Report the malaria status of this cell.
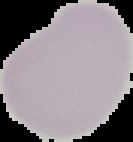
It is uninfected.

Cell region segmented out of the field of view; the surrounding area is masked to black. Image is 133×142 pixels. From a thin blood film.